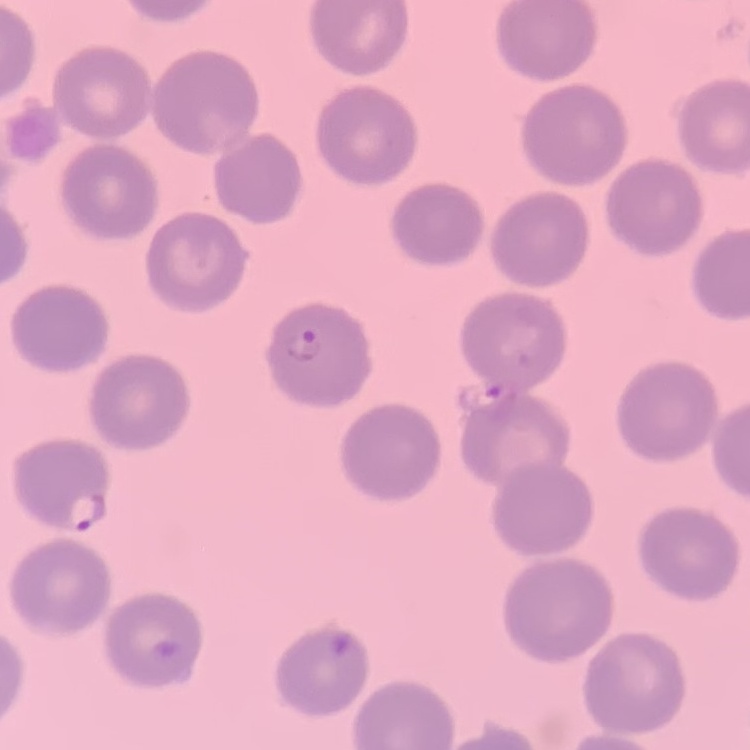

red blood cell morphology = no rouleaux formation
stain = Field's or Giemsa
image type = one tile cut from a larger photomicrograph
preparation = thin peripheral smear